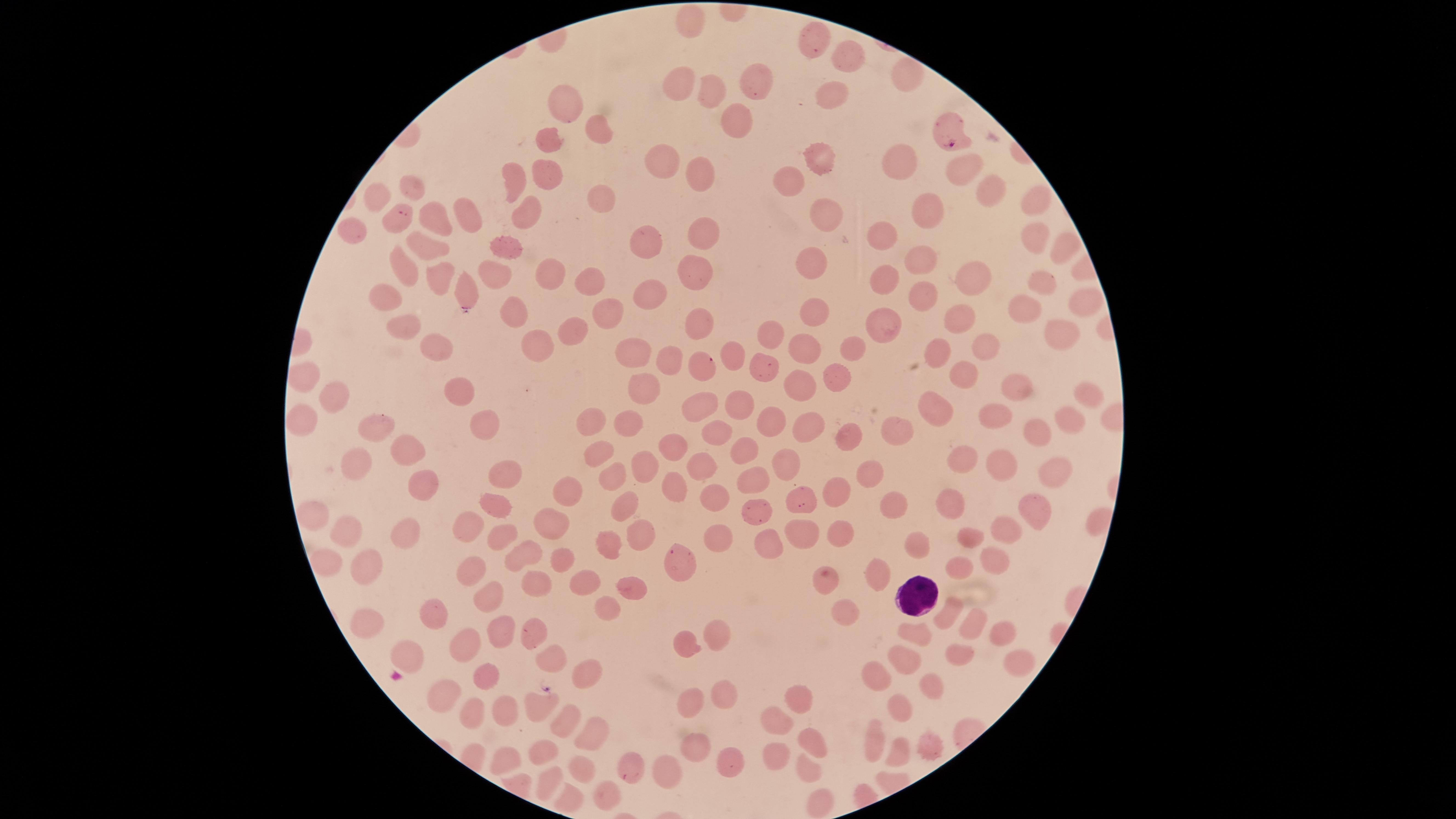
Approximate marker points as (x, y) in pixels. White blood cells: (920, 600). Parasitized red blood cells: (948, 129), (396, 215), (702, 364), (631, 774). Uninfected red blood cells: (692, 23), (813, 43), (845, 59), (905, 76), (749, 87), (678, 89), (704, 91), (832, 93), (567, 102), (731, 120), (597, 131), (549, 144), (819, 159), (896, 161), (660, 164), (544, 170), (962, 171), (697, 173), (789, 180), (513, 185), (988, 190), (373, 202), (596, 202), (1034, 204), (929, 213), (527, 214), (468, 215), (435, 219), (822, 221), (356, 232), (886, 235), (1034, 235), (702, 240), (509, 243), (647, 246), (426, 248), (1064, 248), (919, 264), (493, 267), (810, 267), (701, 270), (408, 271), (550, 273), (974, 274), (439, 277), (886, 280), (588, 281), (1041, 283), (467, 287), (393, 298), (922, 299), (653, 301), (1080, 303), (1022, 311), (816, 313), (514, 314), (611, 316), (957, 319), (698, 320), (402, 323), (573, 326), (885, 326), (1056, 332), (772, 338), (538, 342), (802, 347), (993, 347), (432, 350), (938, 351), (852, 352), (629, 353), (735, 356), (672, 360), (765, 369), (844, 376), (303, 377), (962, 377), (457, 385), (1008, 385), (645, 386), (797, 390), (1082, 395), (331, 404), (737, 406), (697, 407), (937, 413), (994, 413), (1069, 416), (307, 418), (631, 420), (592, 423), (479, 425), (768, 426), (377, 427), (809, 429), (898, 431), (1039, 432), (720, 434), (850, 441), (670, 443), (407, 448), (743, 453), (595, 457), (960, 457), (1004, 460), (355, 465), (699, 465), (787, 465), (645, 466), (1051, 467), (873, 471), (505, 473), (610, 475), (745, 480), (419, 483), (673, 484), (711, 489), (835, 490), (565, 495), (800, 495), (956, 504), (493, 507), (622, 508), (898, 508), (1035, 510), (315, 517), (1006, 528), (471, 529), (545, 529), (407, 530), (841, 531), (971, 534), (499, 535), (635, 535), (800, 535), (344, 538), (719, 538), (917, 539), (762, 541), (608, 542), (524, 555), (559, 557), (996, 557), (366, 560), (676, 566), (963, 566), (471, 567), (877, 572), (583, 580), (827, 581), (534, 586), (625, 587), (492, 590), (606, 606), (846, 607), (945, 613), (430, 615), (362, 625), (974, 625), (528, 627), (997, 630), (500, 631), (916, 631), (718, 633), (464, 643), (683, 645), (405, 653), (548, 656), (966, 656), (910, 657), (1025, 661), (583, 671), (484, 674), (877, 676), (929, 683), (719, 692), (802, 693), (442, 695), (688, 701), (532, 707), (475, 708), (900, 708), (776, 715), (501, 717), (561, 720), (590, 730), (694, 741), (932, 741), (814, 742), (875, 743), (899, 747), (541, 749), (774, 754), (504, 757), (725, 758), (581, 763), (806, 764), (666, 769), (545, 782), (605, 793), (568, 799), (822, 803). Presence: malaria parasites identified. Photographed with a smartphone camera through the microscope eyepiece. One field of view of the specimen. Species: Plasmodium falciparum. The visible region is circular. Image is 1456×819 pixels. Giemsa stain. Thin blood smear.